Comment on the morphology of the erythrocytes.
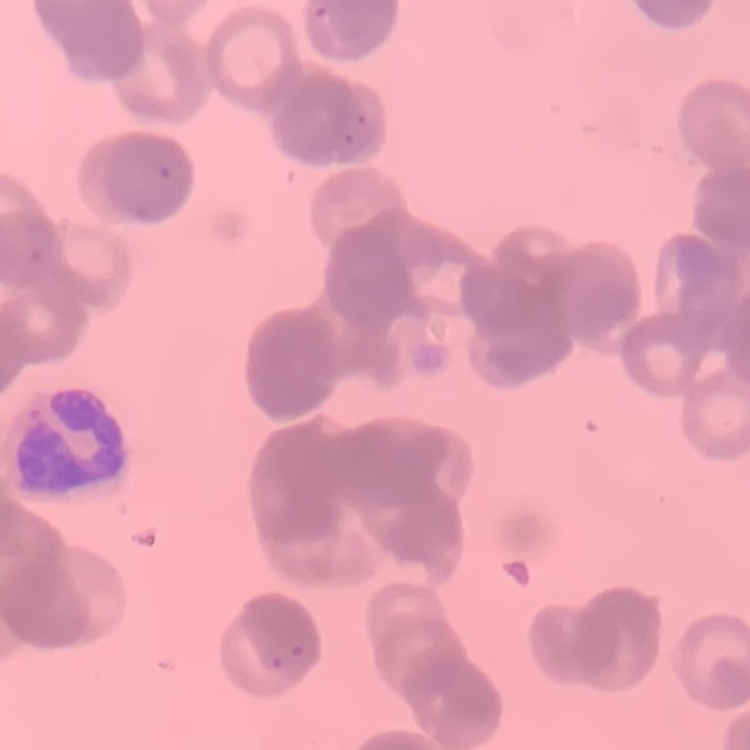
Rouleaux formation.

stain = Field's or Giemsa
image type = square crop of a larger photomicrograph
preparation = thin peripheral smear